Give the position of every Plasmodium parasite, noting whether each is a trophozoite, schizont, or gametocyte.
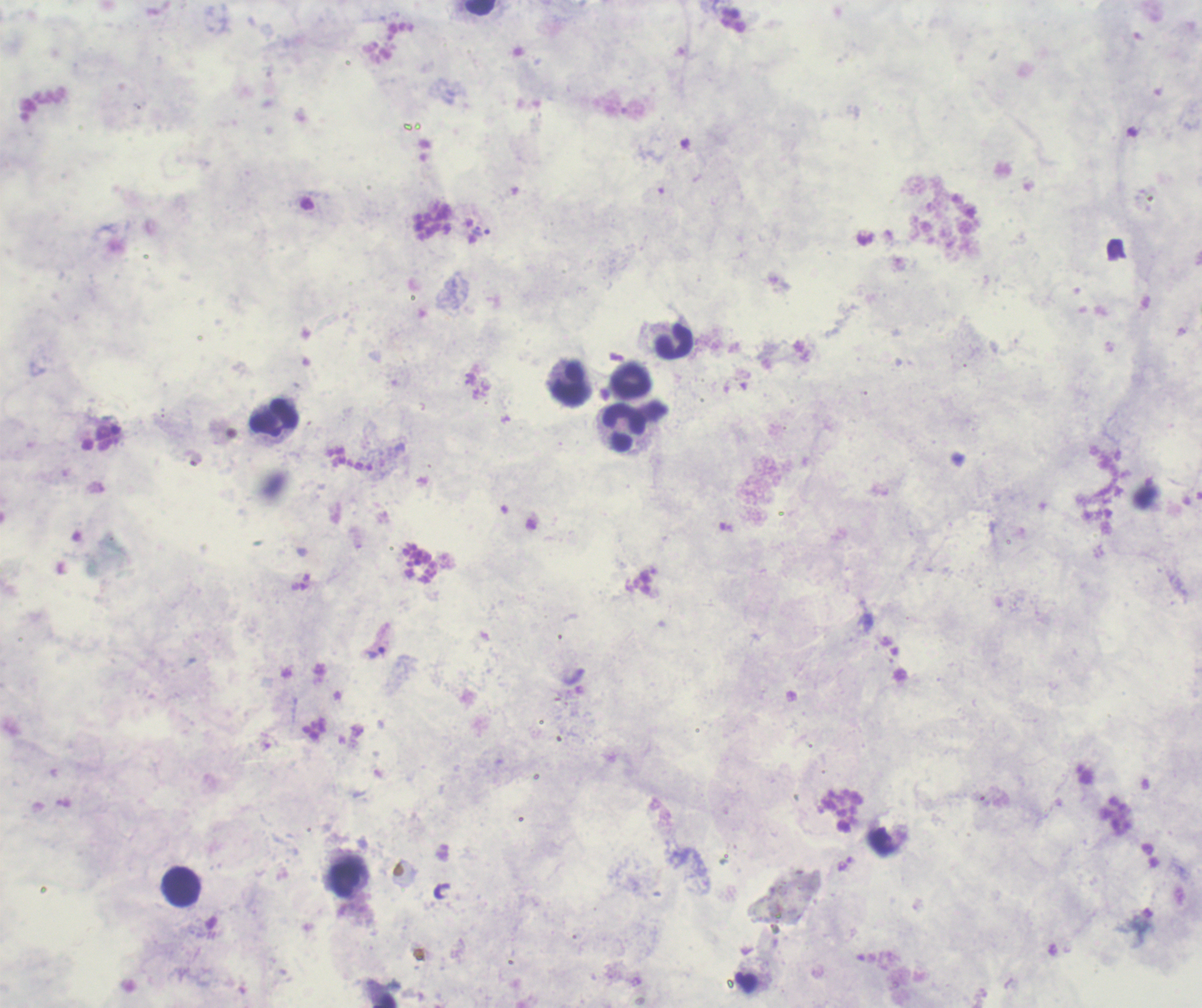
Approximate centers as [x, y] in pixels.
Trophozoites: [480, 232], [376, 652].
No schizont or gametocyte forms observed.

coordinate format = approximate centers as [x, y] in pixels
leukocyte locations = [673, 343], [631, 380], [569, 383], [273, 418], [625, 428], [344, 880], [181, 887]
image size = 1202×1008 pixels
stain = Romanowsky
preparation = thick blood smear
magnification = 100x
context = previously used in an actual diagnosis
field of view = single
background quality = unsatisfactory